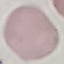
malaria status = uninfected
image type = cell patch, automatically extracted from a larger field of view and resized to 64 × 64 pixels
capture = smartphone through the microscope eyepiece
preparation = thin blood smear
stain = Giemsa